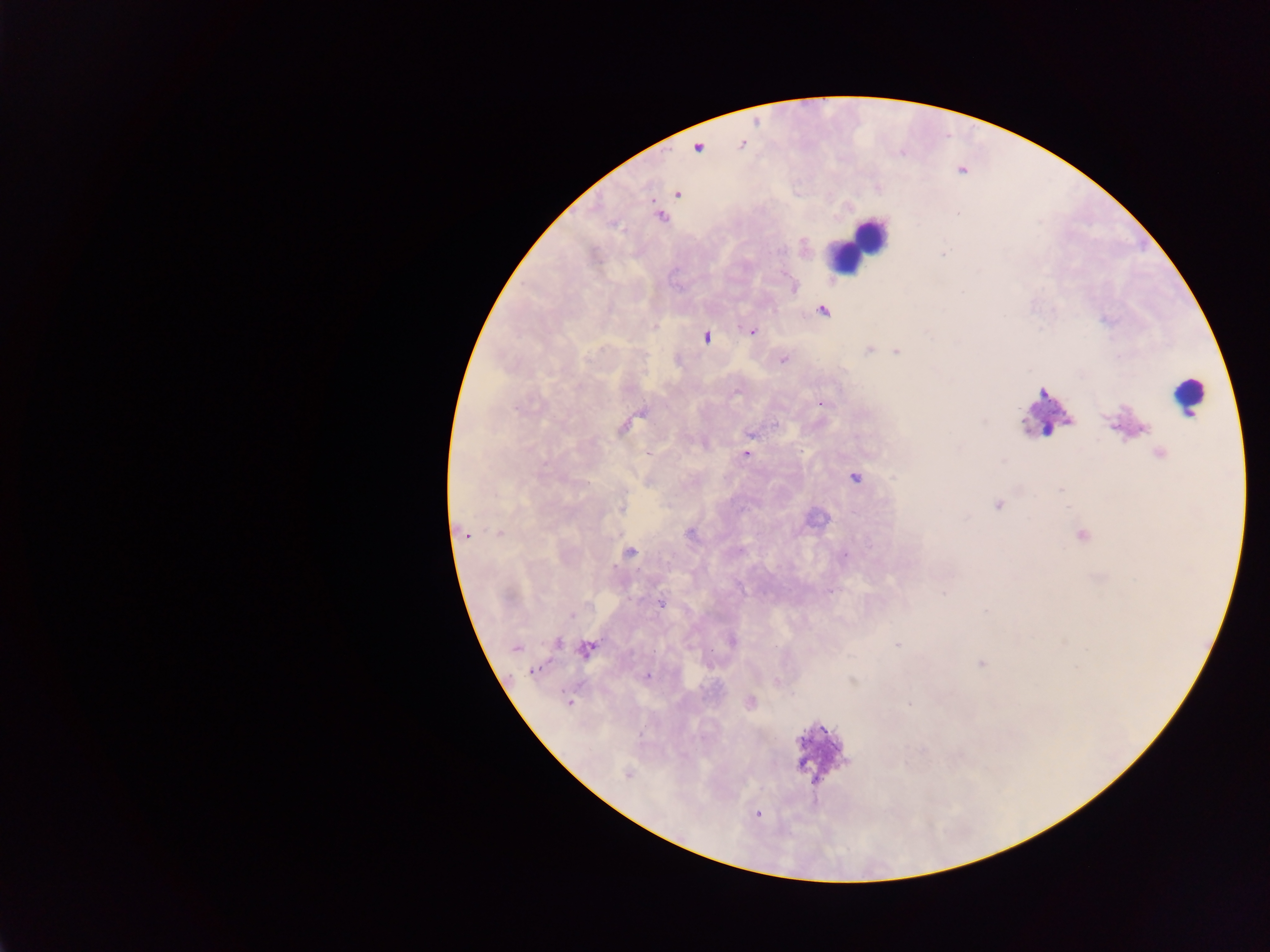
Approximate centers as {x, y} in pixels.
Summary:
  - Leukocyte locations: {855, 241}, {1189, 396}, {1046, 413}, {822, 752}
  - Malaria parasite locations: {742, 145}, {697, 147}, {677, 193}, {660, 216}, {821, 311}, {751, 331}, {705, 337}, {869, 349}, {896, 351}, {783, 359}, {822, 402}, {623, 425}, {751, 433}, {745, 453}, {1158, 454}, {854, 478}, {997, 504}, {465, 533}, {499, 533}, {690, 533}, {1081, 535}, {629, 553}, {844, 556}, {661, 602}, {732, 640}, {558, 643}, {898, 645}, {515, 648}, {586, 648}, {980, 663}, {535, 670}, {647, 676}, {853, 680}, {776, 682}, {569, 702}, {750, 702}, {909, 702}, {628, 774}, {758, 813}
  - Preparation: thick blood smear
  - Capture: mobile-phone photograph through a microscope
  - Image size: 1270×952 pixels
  - Field of view: single
  - Country: Ghana